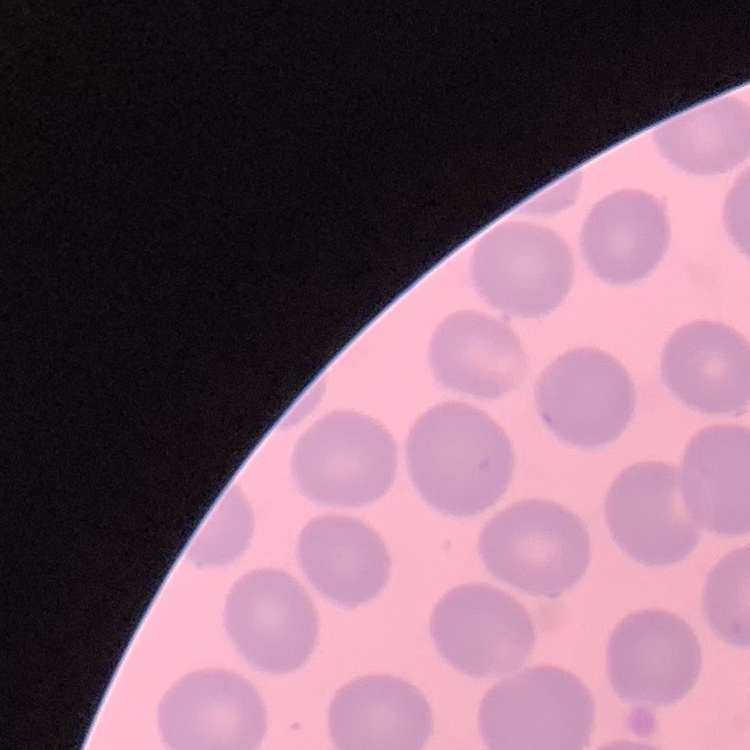

The red blood cells show no rouleaux formation. Thin blood smear. Square crop of a larger photomicrograph. Field's or Giemsa stain.